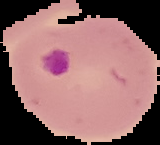
result = malaria parasites detected
image type = segmented cell region with the area outside set to black
image size = 160×145 pixels
preparation = thin blood smear